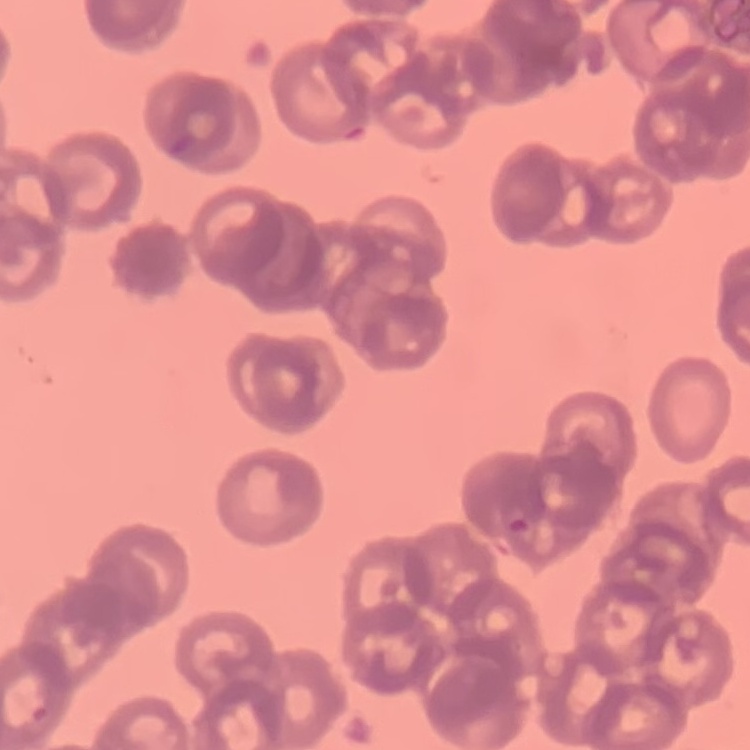
The red blood cells show rouleaux formation. Stained with either Field's or Giemsa. One tile cut from a larger photomicrograph. Thin blood smear.